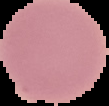
From a thin blood film. Image is 109×106 pixels. Result: negative for Plasmodium parasites. Cell region segmented out of the field of view; the surrounding area is masked to black.